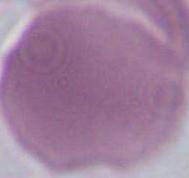 A red blood cell is shown. Micrograph. 1000x magnification.